Report the malaria status of this cell.
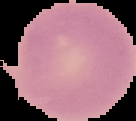
It is uninfected.

Segmented cell region on a black background. From a thin blood film. Image is 136×121 pixels.